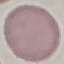
Summary:
  - Result: no malaria parasites seen
  - Preparation: thin smear
  - Stain: Giemsa
  - Capture: smartphone through the microscope eyepiece
  - Image type: automatically extracted cell patch, resized to 64 × 64 pixels